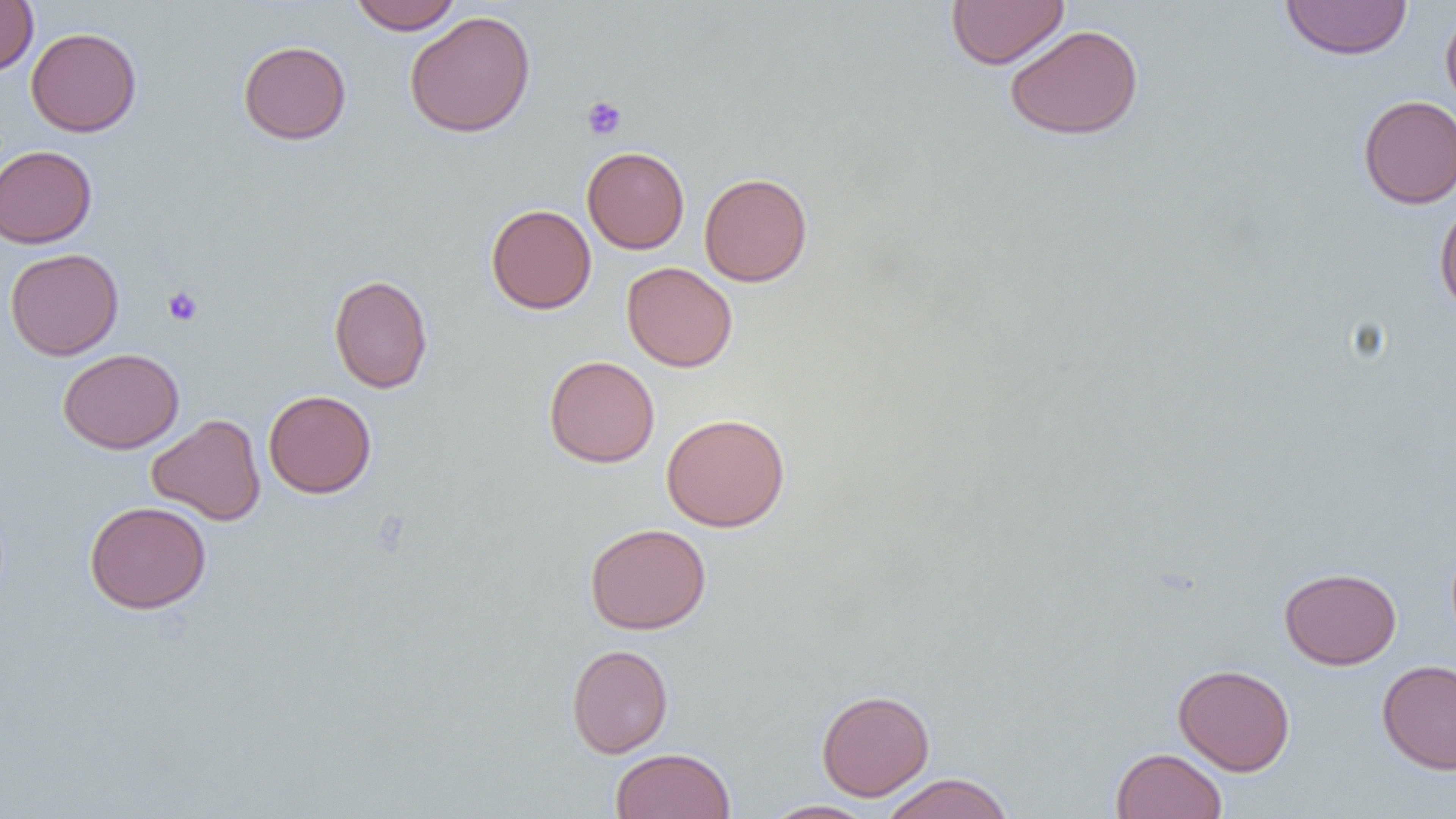
Summary:
  - Coordinate format: approximate bounding boxes as (x1,y1)-(x2,y2) corner pairs in pixels
  - Uninfected red blood cell locations: (348,0)-(463,33), (946,0)-(1069,69), (0,1)-(38,76), (1280,1)-(1413,60), (1440,5)-(1456,117), (404,11)-(536,138), (1005,24)-(1144,140), (26,27)-(142,137), (238,40)-(352,145), (1358,95)-(1456,208), (0,145)-(97,248), (582,146)-(690,254), (698,172)-(813,287), (1434,198)-(1456,319), (486,204)-(597,314), (4,248)-(124,360), (622,262)-(737,372), (329,274)-(433,394), (57,348)-(185,454), (544,355)-(660,468), (263,390)-(376,498), (661,413)-(790,532), (146,414)-(265,525), (84,500)-(211,614), (584,523)-(712,635), (1279,567)-(1402,670), (566,643)-(674,758), (1377,660)-(1456,774), (1173,664)-(1295,776), (816,689)-(935,801), (1111,747)-(1228,819), (610,748)-(736,818), (881,773)-(1014,819), (761,799)-(878,818)
  - Platelet locations: (582,96)-(627,140), (163,286)-(203,326)
  - Slide-level diagnosis: no evidence of blood parasites
  - Field of view: one of a larger specimen
  - Image size: 1456×819 pixels
  - Modality: optical microscopy
  - Preparation: thin blood film
  - Magnification: 1000x